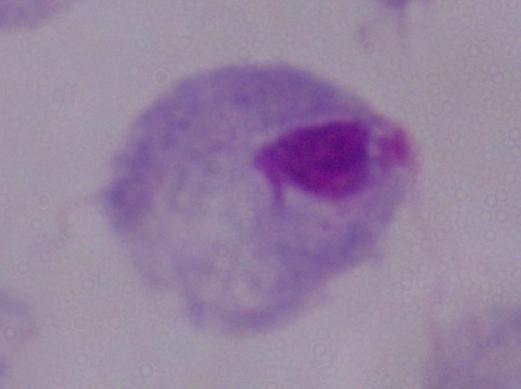

identification: trichomonad
magnification: 1000x
modality: micrograph